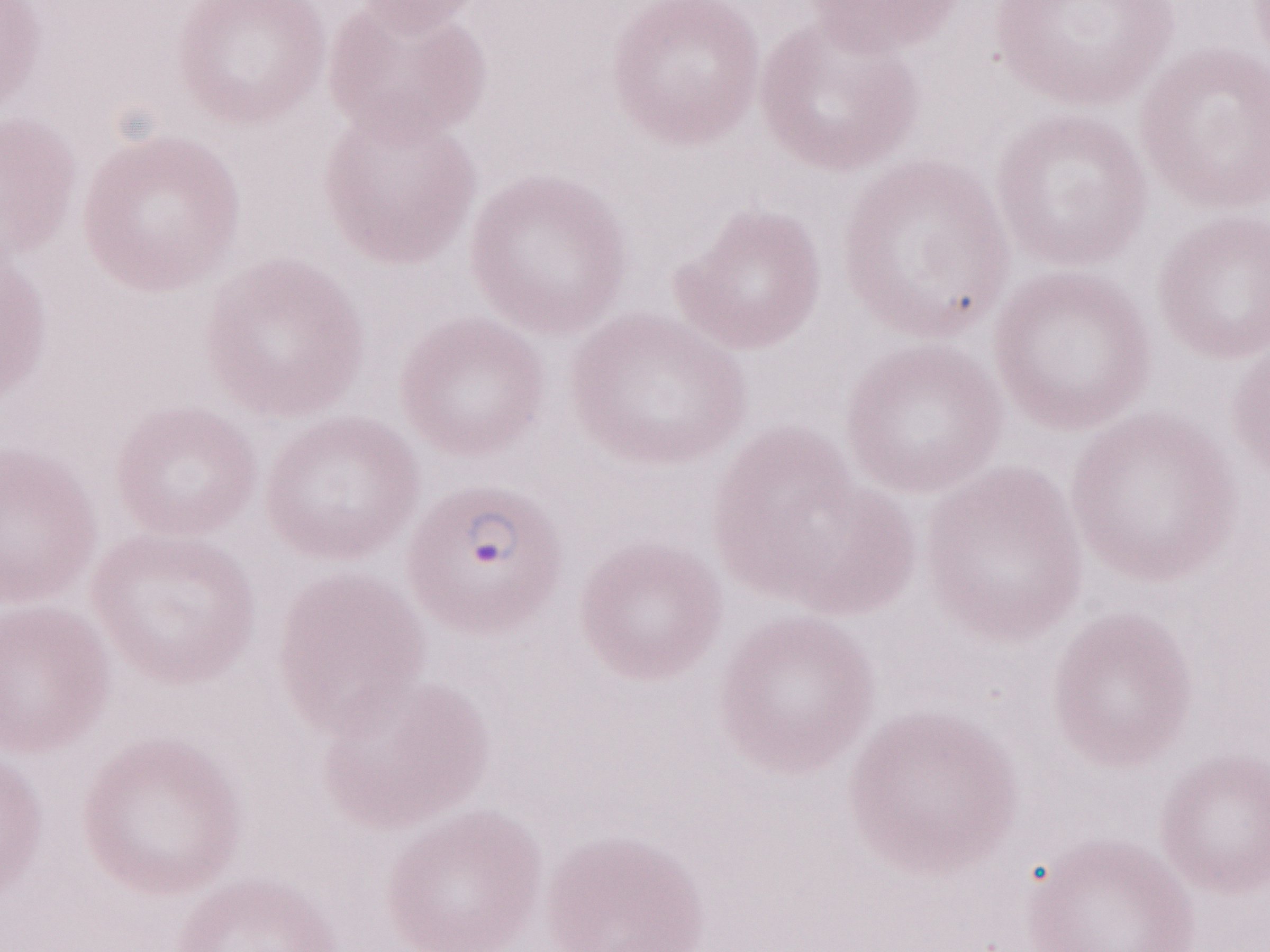 One field of this slide. 1,000x magnification. Thin peripheral-blood smear. May-Grünwald-Giemsa stain. Image is 1270×952 pixels. Patient diagnosis: malaria infection. Olympus BX43 microscope and DP73 digital camera.